Classify this cell by malaria status.
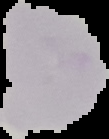
Uninfected.

preparation = thin blood film
image size = 109×139 pixels
image type = cell region segmented out of the field of view; surrounding area masked to black